Report the malaria status of this cell.
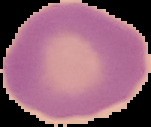

Uninfected.

Summary:
  - Preparation: thin blood smear
  - Image size: 151×127 pixels
  - Image type: cell region segmented out of the field of view; surrounding area masked to black